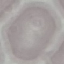
Result: no malaria parasites seen. Giemsa stain. Cell patch, automatically extracted from a larger field of view and resized to 64 × 64 pixels. Thin smear of blood. Acquired by smartphone through the microscope eyepiece.